Assess for Plasmodium parasites.
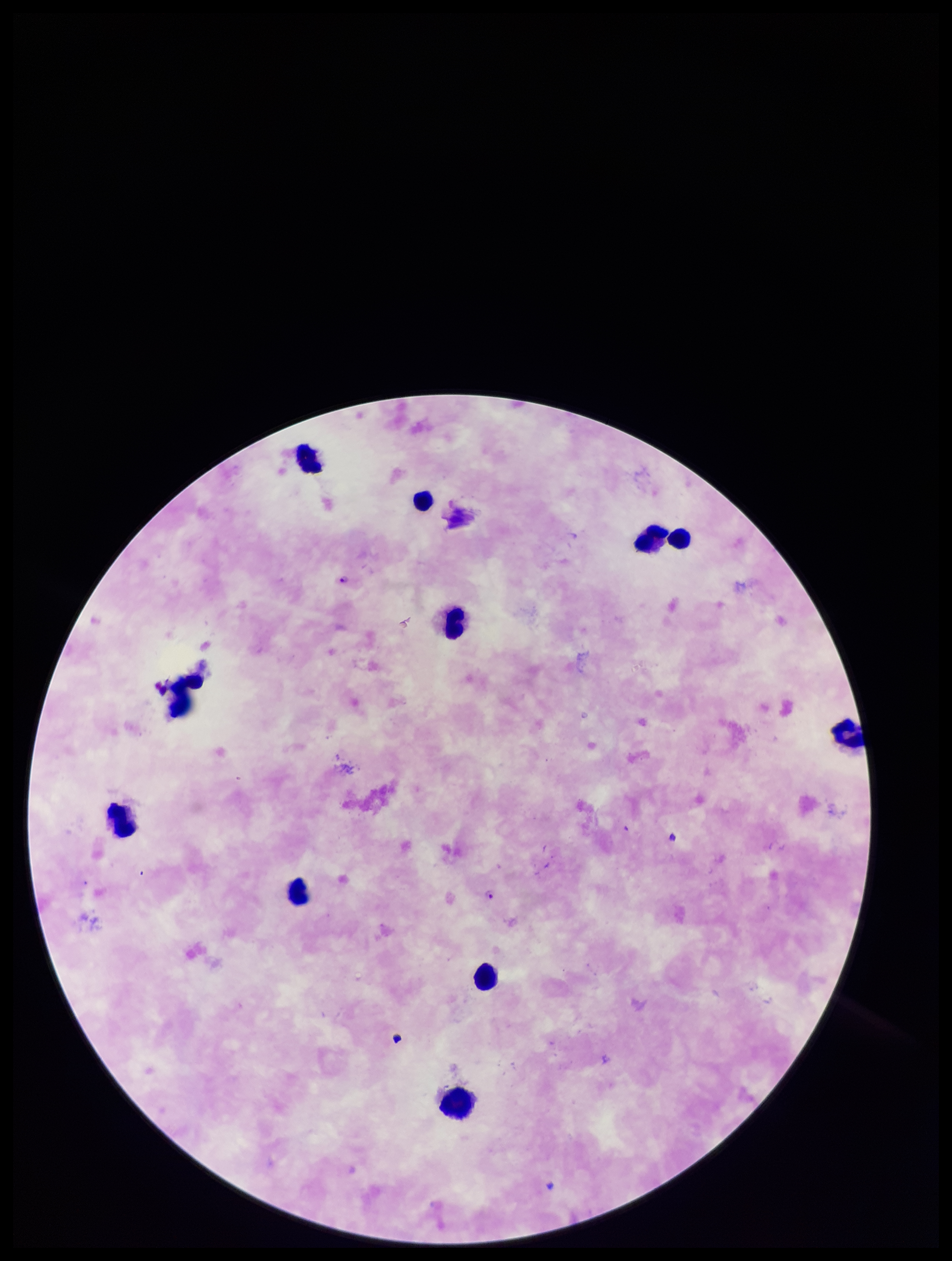

Seen.

{
  "field_of_view": "single",
  "stain": "Giemsa",
  "preparation": "thick blood smear",
  "patient_malaria_status": "positive",
  "parasite_count": 2,
  "capture": "smartphone photograph through the microscope eyepiece",
  "image_size": "952×1261 pixels",
  "species_reported_for_this_patient": "Plasmodium falciparum",
  "leukocyte_count": 11
}